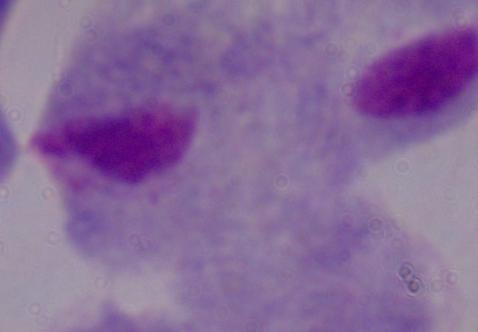
Captured at 1000x magnification. A trichomonad is shown. Micrograph.